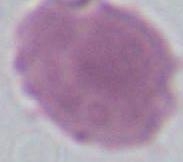

Micrograph. A red blood cell is seen. 1000x magnification.